Point out each malaria parasite and each leukocyte.
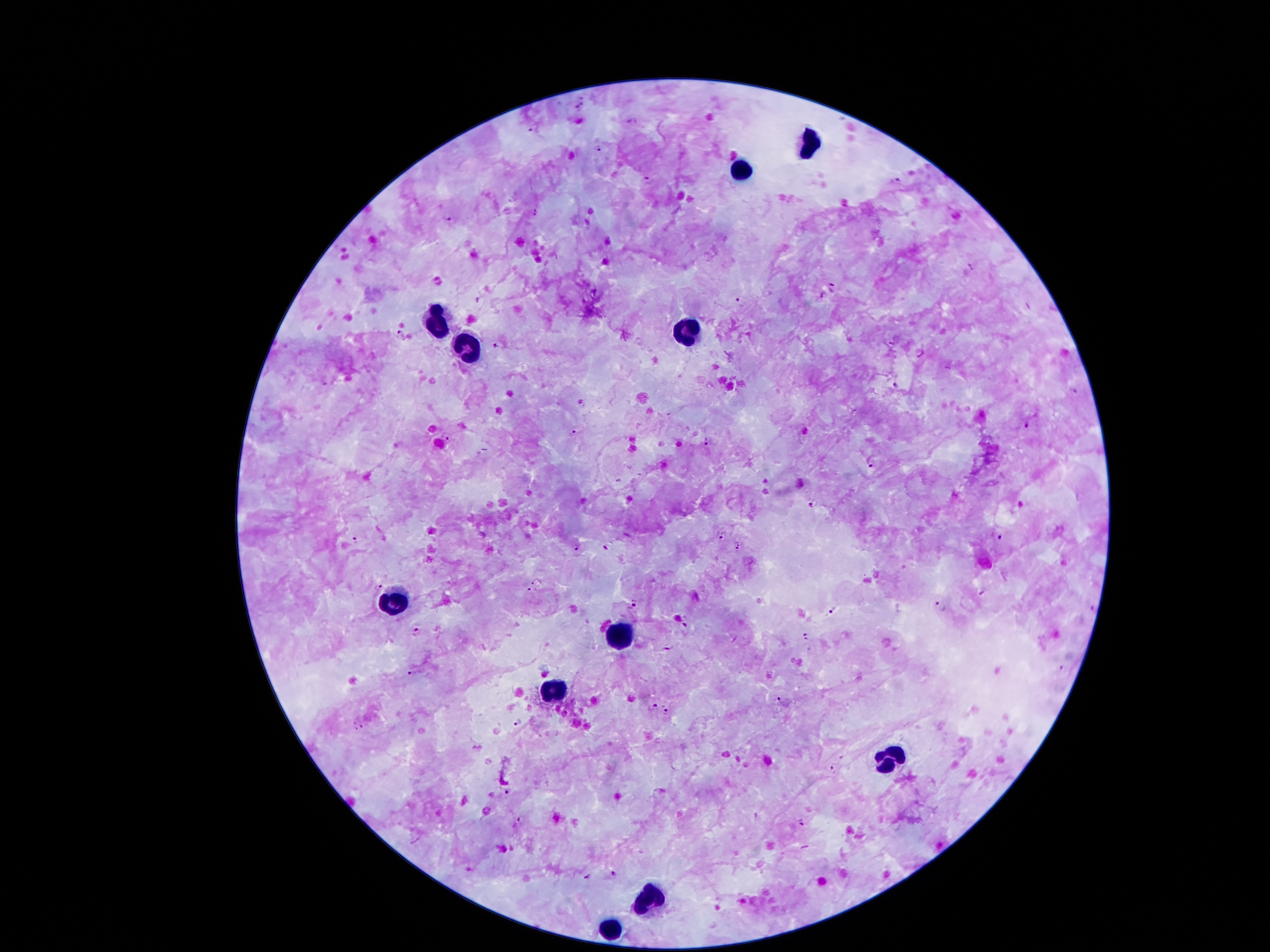
Approximate object centers, in pixels from the top-left corner.
Malaria parasites: (x=579, y=105), (x=633, y=121), (x=533, y=129), (x=598, y=148), (x=651, y=181), (x=896, y=183), (x=444, y=215), (x=970, y=269), (x=832, y=289), (x=741, y=303), (x=401, y=334), (x=497, y=345), (x=891, y=345), (x=920, y=352), (x=896, y=385), (x=1074, y=390), (x=1028, y=423), (x=575, y=432), (x=446, y=438), (x=706, y=440), (x=871, y=461), (x=811, y=505), (x=722, y=534), (x=1000, y=537), (x=356, y=540), (x=738, y=546), (x=609, y=547), (x=576, y=548), (x=538, y=580), (x=377, y=585), (x=531, y=591), (x=981, y=592), (x=634, y=602), (x=940, y=606), (x=834, y=612), (x=684, y=624), (x=414, y=630), (x=808, y=635), (x=667, y=649), (x=1063, y=669), (x=414, y=671), (x=779, y=698), (x=650, y=707), (x=666, y=710), (x=516, y=721), (x=358, y=725), (x=833, y=770), (x=509, y=789), (x=522, y=819), (x=802, y=821), (x=612, y=873), (x=588, y=877).
Leukocytes: (x=808, y=147), (x=740, y=173), (x=440, y=324), (x=686, y=337), (x=468, y=352), (x=393, y=599), (x=617, y=632), (x=554, y=692), (x=890, y=756), (x=649, y=896), (x=610, y=929).

magnification: 100x
image_size: 1270×952 pixels
capture: smartphone camera through the microscope eyepiece
preparation: thick blood smear
field_of_view: one from this slide
patient_malaria_status: infected with Plasmodium falciparum
stain: Giemsa